Identify the blood parasite species.
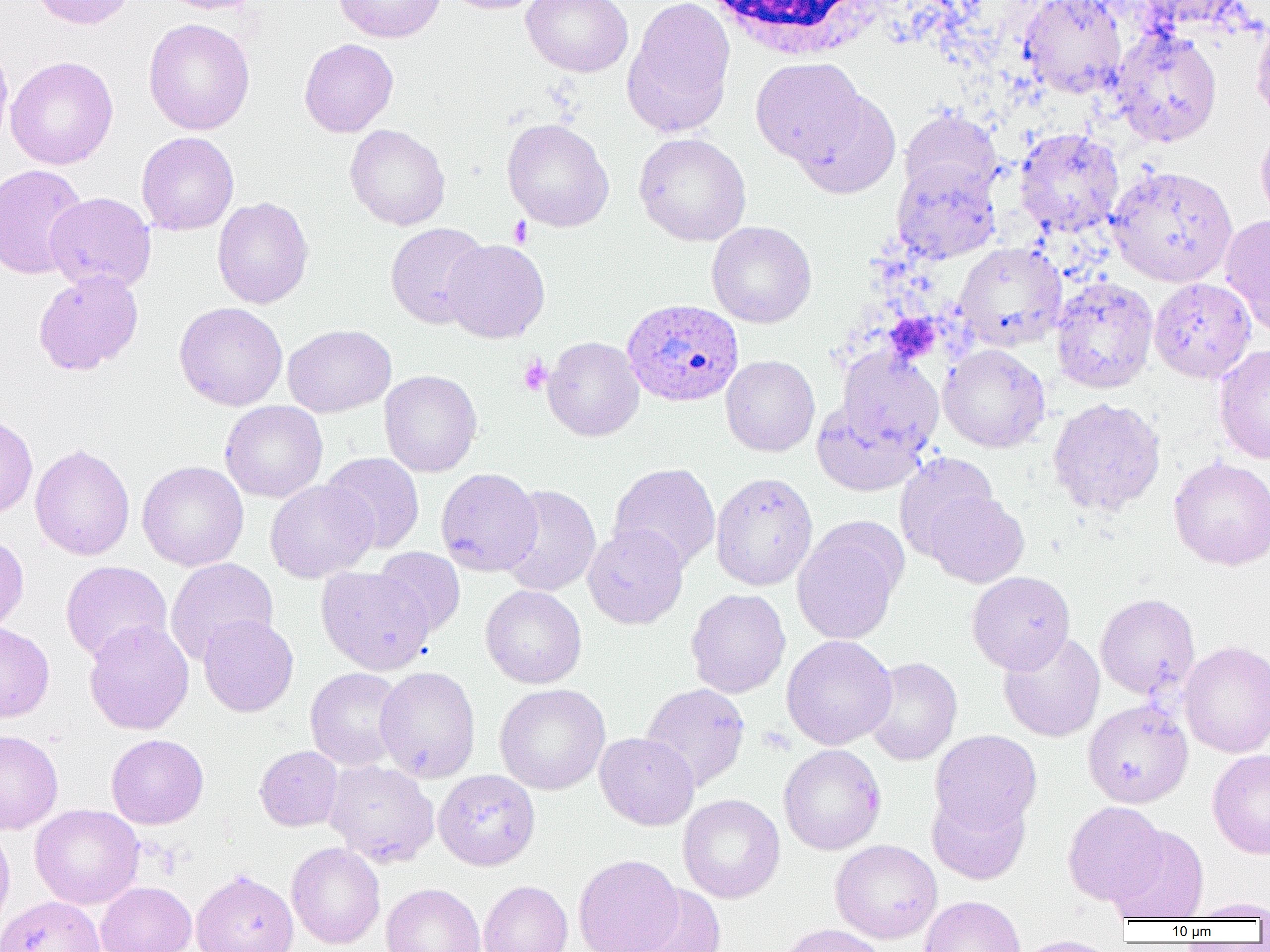
Plasmodium ovale.

Approximate bounding boxes as named x1/y1/x2/y2 corners in pixels. Uninfected red blood cell locations: (x1=28, y1=0, x2=136, y2=29), (x1=155, y1=0, x2=264, y2=14), (x1=334, y1=0, x2=446, y2=43), (x1=442, y1=0, x2=547, y2=14), (x1=521, y1=0, x2=633, y2=77), (x1=623, y1=0, x2=735, y2=138), (x1=1019, y1=0, x2=1128, y2=98), (x1=1136, y1=0, x2=1251, y2=31), (x1=1251, y1=14, x2=1270, y2=127), (x1=143, y1=18, x2=255, y2=135), (x1=1111, y1=28, x2=1223, y2=147), (x1=0, y1=36, x2=13, y2=154), (x1=299, y1=38, x2=398, y2=137), (x1=5, y1=56, x2=118, y2=170), (x1=750, y1=57, x2=866, y2=165), (x1=792, y1=90, x2=901, y2=198), (x1=899, y1=108, x2=1002, y2=202), (x1=502, y1=118, x2=614, y2=232), (x1=1255, y1=122, x2=1270, y2=230), (x1=345, y1=124, x2=450, y2=230), (x1=1014, y1=127, x2=1125, y2=238), (x1=136, y1=132, x2=239, y2=235), (x1=633, y1=132, x2=752, y2=246), (x1=892, y1=160, x2=1001, y2=263), (x1=1, y1=164, x2=88, y2=280), (x1=1107, y1=165, x2=1238, y2=287), (x1=44, y1=192, x2=156, y2=293), (x1=212, y1=196, x2=314, y2=309), (x1=1219, y1=213, x2=1270, y2=338), (x1=707, y1=220, x2=817, y2=328), (x1=385, y1=222, x2=489, y2=328), (x1=441, y1=239, x2=550, y2=343), (x1=954, y1=242, x2=1067, y2=350), (x1=33, y1=269, x2=143, y2=375), (x1=1051, y1=277, x2=1158, y2=393), (x1=1149, y1=277, x2=1256, y2=382), (x1=174, y1=302, x2=288, y2=411), (x1=283, y1=324, x2=396, y2=417), (x1=543, y1=336, x2=644, y2=442), (x1=939, y1=343, x2=1050, y2=452), (x1=1213, y1=344, x2=1270, y2=464), (x1=837, y1=349, x2=944, y2=453), (x1=720, y1=355, x2=820, y2=457), (x1=379, y1=369, x2=482, y2=477), (x1=1048, y1=397, x2=1166, y2=516), (x1=220, y1=400, x2=328, y2=503), (x1=812, y1=400, x2=926, y2=496), (x1=0, y1=413, x2=38, y2=518), (x1=30, y1=443, x2=135, y2=560), (x1=321, y1=452, x2=424, y2=554), (x1=894, y1=452, x2=1000, y2=561), (x1=1168, y1=456, x2=1270, y2=570), (x1=137, y1=461, x2=249, y2=571), (x1=608, y1=463, x2=721, y2=573), (x1=436, y1=467, x2=542, y2=576), (x1=710, y1=472, x2=818, y2=591), (x1=265, y1=480, x2=377, y2=583), (x1=499, y1=484, x2=601, y2=597), (x1=925, y1=491, x2=1029, y2=588), (x1=792, y1=518, x2=906, y2=647), (x1=583, y1=524, x2=689, y2=629), (x1=0, y1=534, x2=28, y2=636), (x1=372, y1=546, x2=466, y2=638), (x1=165, y1=558, x2=278, y2=665), (x1=60, y1=561, x2=172, y2=664), (x1=316, y1=566, x2=434, y2=674), (x1=967, y1=571, x2=1075, y2=674), (x1=480, y1=585, x2=587, y2=688), (x1=686, y1=589, x2=790, y2=698), (x1=1095, y1=593, x2=1199, y2=699), (x1=198, y1=614, x2=299, y2=717), (x1=83, y1=619, x2=194, y2=735), (x1=0, y1=623, x2=54, y2=722), (x1=998, y1=632, x2=1105, y2=742), (x1=781, y1=634, x2=897, y2=750), (x1=1179, y1=640, x2=1270, y2=758), (x1=863, y1=656, x2=963, y2=766), (x1=375, y1=666, x2=480, y2=783), (x1=305, y1=667, x2=407, y2=771), (x1=494, y1=683, x2=611, y2=795), (x1=640, y1=683, x2=750, y2=791), (x1=1082, y1=699, x2=1193, y2=808), (x1=0, y1=729, x2=63, y2=835), (x1=930, y1=730, x2=1042, y2=834), (x1=594, y1=732, x2=699, y2=831), (x1=106, y1=733, x2=209, y2=829), (x1=778, y1=744, x2=886, y2=855), (x1=255, y1=745, x2=343, y2=831), (x1=1208, y1=749, x2=1270, y2=859), (x1=323, y1=759, x2=439, y2=867), (x1=433, y1=769, x2=540, y2=871), (x1=927, y1=790, x2=1030, y2=885), (x1=678, y1=794, x2=785, y2=903), (x1=1062, y1=801, x2=1168, y2=906), (x1=30, y1=804, x2=144, y2=909), (x1=0, y1=822, x2=15, y2=937), (x1=1108, y1=826, x2=1209, y2=921), (x1=830, y1=839, x2=942, y2=944), (x1=286, y1=842, x2=385, y2=949), (x1=573, y1=854, x2=683, y2=952), (x1=191, y1=870, x2=298, y2=952), (x1=478, y1=880, x2=573, y2=952), (x1=96, y1=881, x2=197, y2=952), (x1=381, y1=882, x2=485, y2=952), (x1=625, y1=885, x2=726, y2=952), (x1=920, y1=895, x2=1025, y2=952), (x1=0, y1=896, x2=106, y2=952), (x1=1183, y1=897, x2=1270, y2=921), (x1=773, y1=923, x2=888, y2=952), (x1=1009, y1=935, x2=1118, y2=952). Platelet locations: (x1=508, y1=216, x2=533, y2=247), (x1=882, y1=314, x2=938, y2=354), (x1=518, y1=355, x2=552, y2=395). Plasmodium ovale-infected red blood cell locations: (x1=621, y1=298, x2=743, y2=408). White blood cell locations: (x1=702, y1=0, x2=885, y2=61). 1000x magnification. Image is 1270×952 pixels. Thin blood smear. Optical microscopy. One field of a larger specimen.